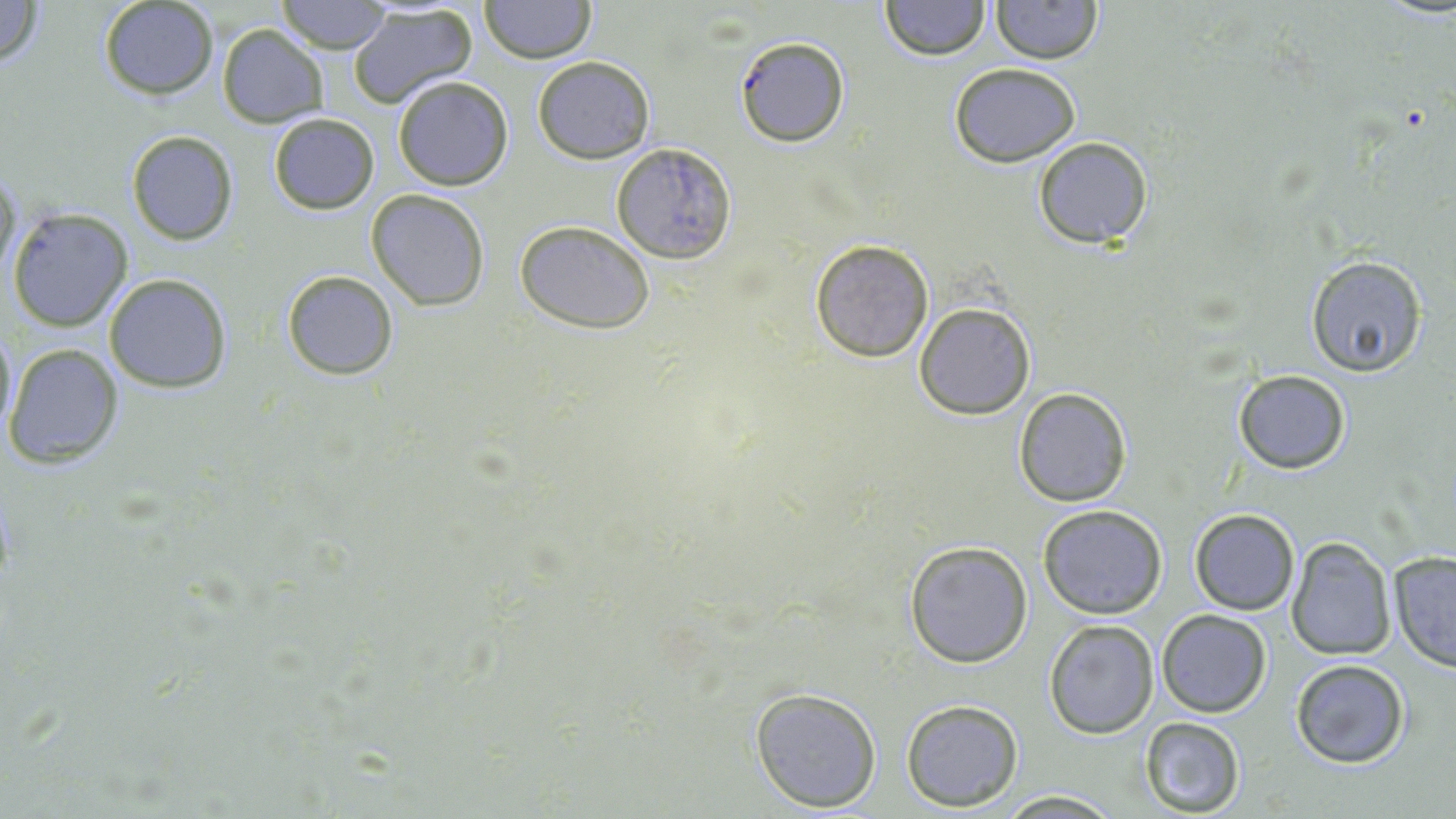

Summary:
  - Coordinate format: approximate bounding boxes as named x1/y1/x2/y2 corners in pixels
  - Uninfected red blood cell locations: (x1=0, y1=0, x2=47, y2=67), (x1=276, y1=0, x2=396, y2=53), (x1=480, y1=0, x2=594, y2=65), (x1=99, y1=1, x2=217, y2=99), (x1=880, y1=1, x2=989, y2=61), (x1=990, y1=1, x2=1102, y2=65), (x1=346, y1=6, x2=479, y2=108), (x1=217, y1=23, x2=329, y2=128), (x1=532, y1=56, x2=654, y2=164), (x1=950, y1=61, x2=1080, y2=167), (x1=392, y1=75, x2=514, y2=191), (x1=267, y1=113, x2=380, y2=215), (x1=125, y1=129, x2=240, y2=247), (x1=1032, y1=135, x2=1153, y2=248), (x1=612, y1=142, x2=738, y2=265), (x1=0, y1=165, x2=20, y2=282), (x1=366, y1=189, x2=491, y2=312), (x1=7, y1=207, x2=134, y2=332), (x1=515, y1=221, x2=657, y2=334), (x1=810, y1=239, x2=936, y2=361), (x1=1305, y1=255, x2=1428, y2=376), (x1=281, y1=270, x2=399, y2=379), (x1=104, y1=273, x2=232, y2=392), (x1=915, y1=302, x2=1035, y2=419), (x1=1, y1=323, x2=16, y2=436), (x1=4, y1=344, x2=123, y2=467), (x1=1232, y1=369, x2=1353, y2=475), (x1=1013, y1=387, x2=1131, y2=506), (x1=1038, y1=504, x2=1168, y2=620), (x1=1189, y1=507, x2=1300, y2=615), (x1=1286, y1=536, x2=1397, y2=660), (x1=904, y1=539, x2=1033, y2=668), (x1=1386, y1=550, x2=1456, y2=672), (x1=1155, y1=608, x2=1271, y2=717), (x1=1043, y1=619, x2=1159, y2=737), (x1=1289, y1=659, x2=1411, y2=770), (x1=749, y1=685, x2=883, y2=813), (x1=901, y1=698, x2=1024, y2=812), (x1=1139, y1=716, x2=1244, y2=816), (x1=996, y1=790, x2=1121, y2=818)
  - Plasmodium falciparum-infected red blood cell locations: (x1=734, y1=35, x2=849, y2=147)
  - Slide-level diagnosis: Plasmodium falciparum
  - Field of view: single
  - Magnification: 1000x
  - Stain: May-Grünwald-Giemsa
  - Preparation: thin blood smear
  - Image size: 1456×819 pixels
  - Modality: optical microscopy